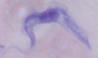
modality = micrograph
identification = trypanosome
magnification = 1000x